Classify this cell by malaria status.
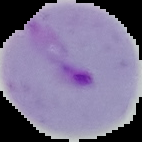

Parasitized.

Image is 142×142 pixels. From a thin blood film. Segmented cell region on a black background.